Locate every Plasmodium parasite.
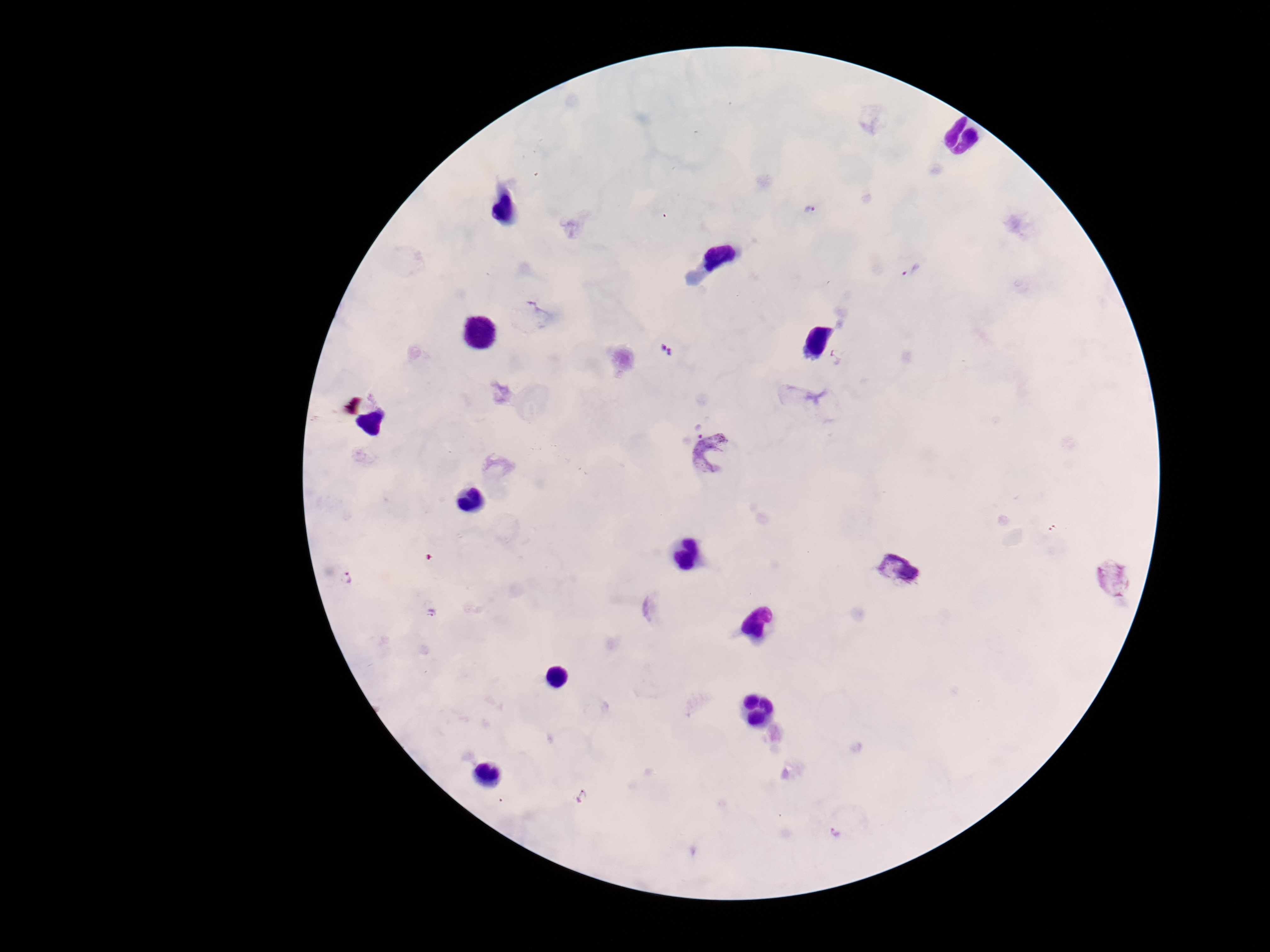
Approximate centers as {x, y} in pixels.
Plasmodium parasites: {809, 211}, {909, 270}, {667, 351}, {834, 359}, {693, 424}, {720, 460}, {899, 569}, {1112, 578}, {346, 579}, {431, 612}, {833, 832}.

Summary:
  - Stain: Giemsa
  - Capture: smartphone camera through the microscope eyepiece
  - Preparation: thick blood smear
  - Image size: 1270×952 pixels
  - Patient malaria status: positive
  - Field of view: single
  - Magnification: 100x